Point out each malaria parasite.
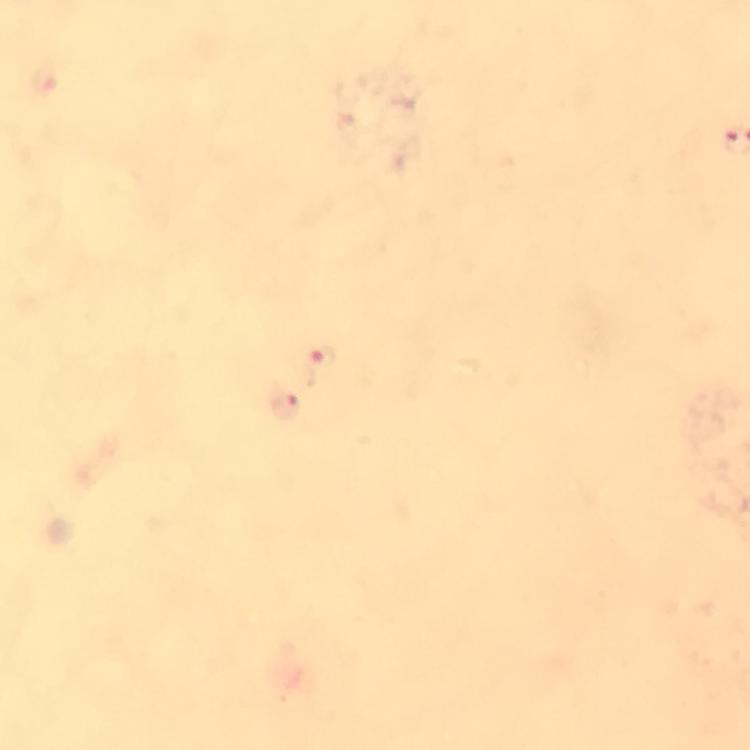
Approximate centers as [x, y] in pixels.
Malaria parasites: [324, 368], [286, 407].

Summary:
  - Stain: Giemsa
  - Cropped from: one field of view
  - Magnification: 100x
  - Preparation: thick blood smear
  - Capture: smartphone camera through the microscope
  - Image size: 750×750 pixels
  - Context: from a diagnostic examination for malaria
  - Immersion oil: used